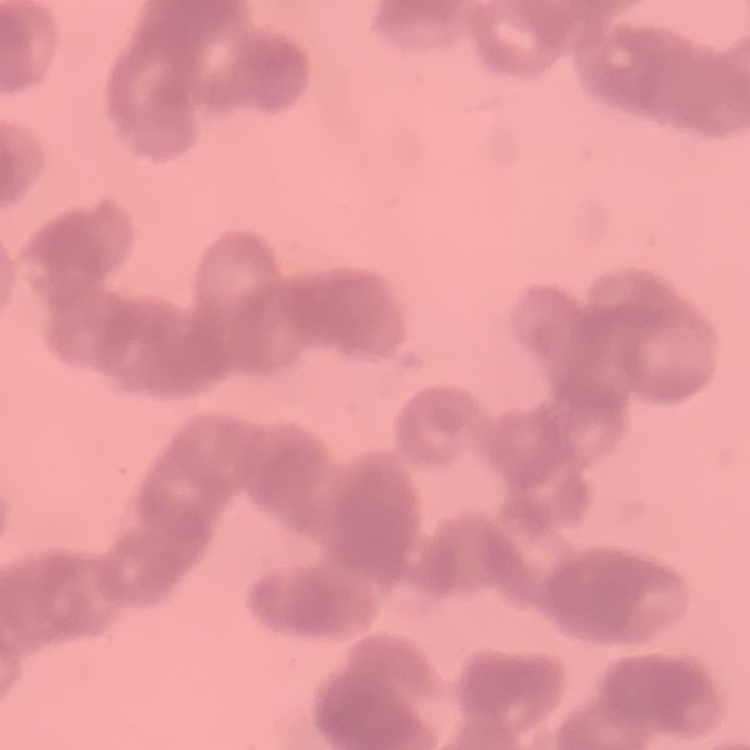
The erythrocytes exhibit rouleaux formation. Thin peripheral smear. Square crop of a larger photomicrograph. Field's or Giemsa stain.